Classify this cell by malaria status.
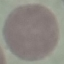
Uninfected.

Summary:
  - Preparation: thin blood film
  - Image type: cell patch, automatically extracted from a larger field of view and resized to 64 × 64 pixels
  - Stain: Giemsa
  - Capture: smartphone camera at the microscope eyepiece